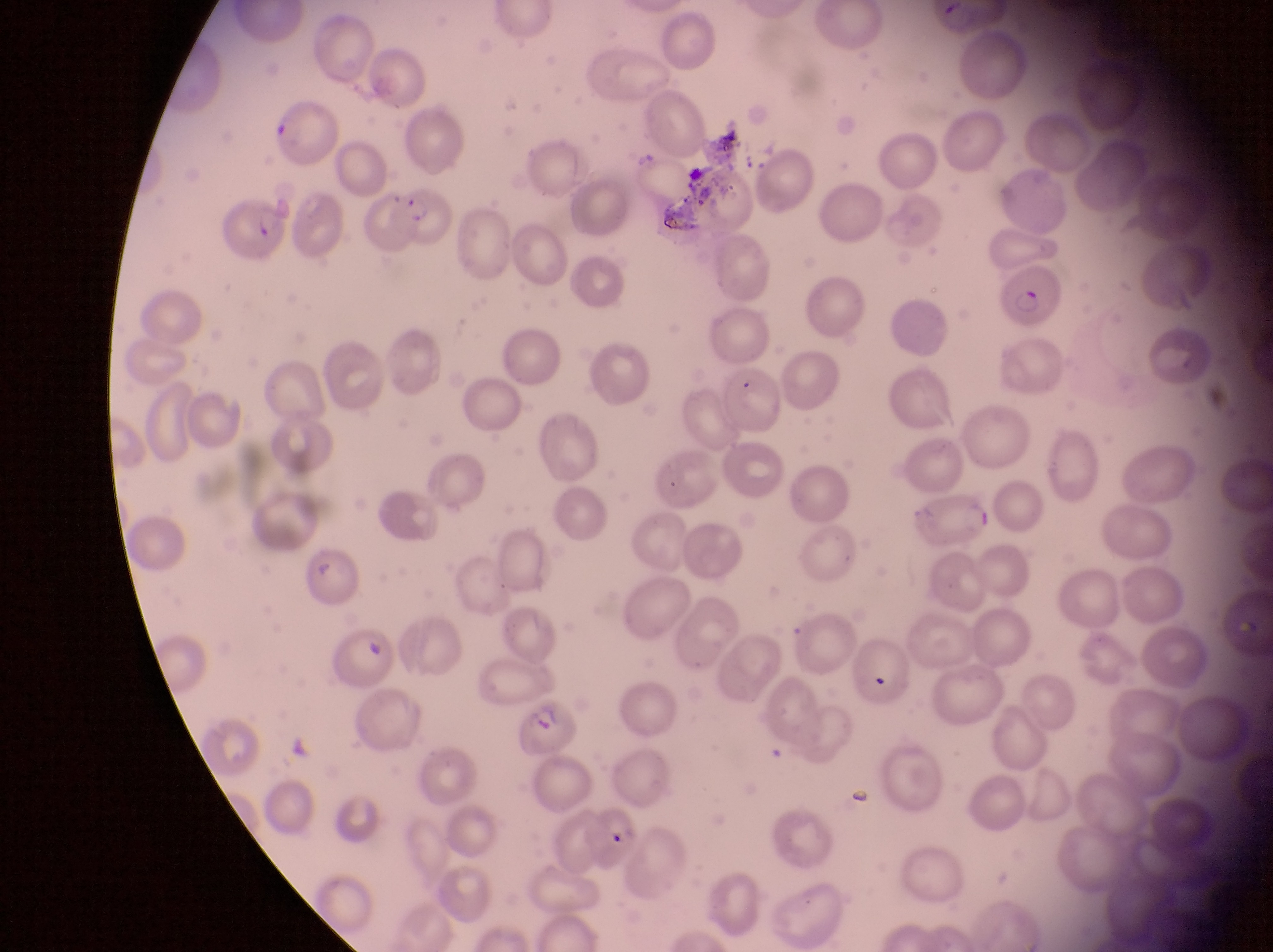

country: Uganda
preparation: thin blood smear
parasitised_red_blood_cell_locations: 'approximate bounding boxes as {left, top, right, bottom} in pixels: {274, 108, 346, 166}, {372, 185, 455, 252}, {220, 192, 294, 269}, {1003, 265, 1065, 333}, {908, 499, 998, 549}, {512, 699, 581, 759}'
image_size: 1273×952 pixels
capture: smartphone photograph through the eyepiece of an Olympus CX-23 microscope
field_of_view: single
magnification: 1000x